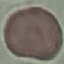
Summary:
  - Malaria status: uninfected
  - Capture: smartphone through the microscope eyepiece
  - Stain: Giemsa
  - Image type: cell patch, automatically extracted from a larger field of view and resized to 64 × 64 pixels
  - Preparation: thin blood smear